Assess this cell for malaria.
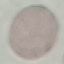

It is uninfected.

Summary:
  - Image type: automatically extracted cell patch, resized to 64 × 64 pixels
  - Stain: Giemsa
  - Preparation: thin smear
  - Capture: smartphone camera at the microscope eyepiece